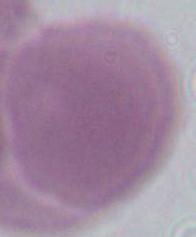

{
  "identification": "red blood cell",
  "modality": "photomicrograph",
  "magnification": "1000x"
}